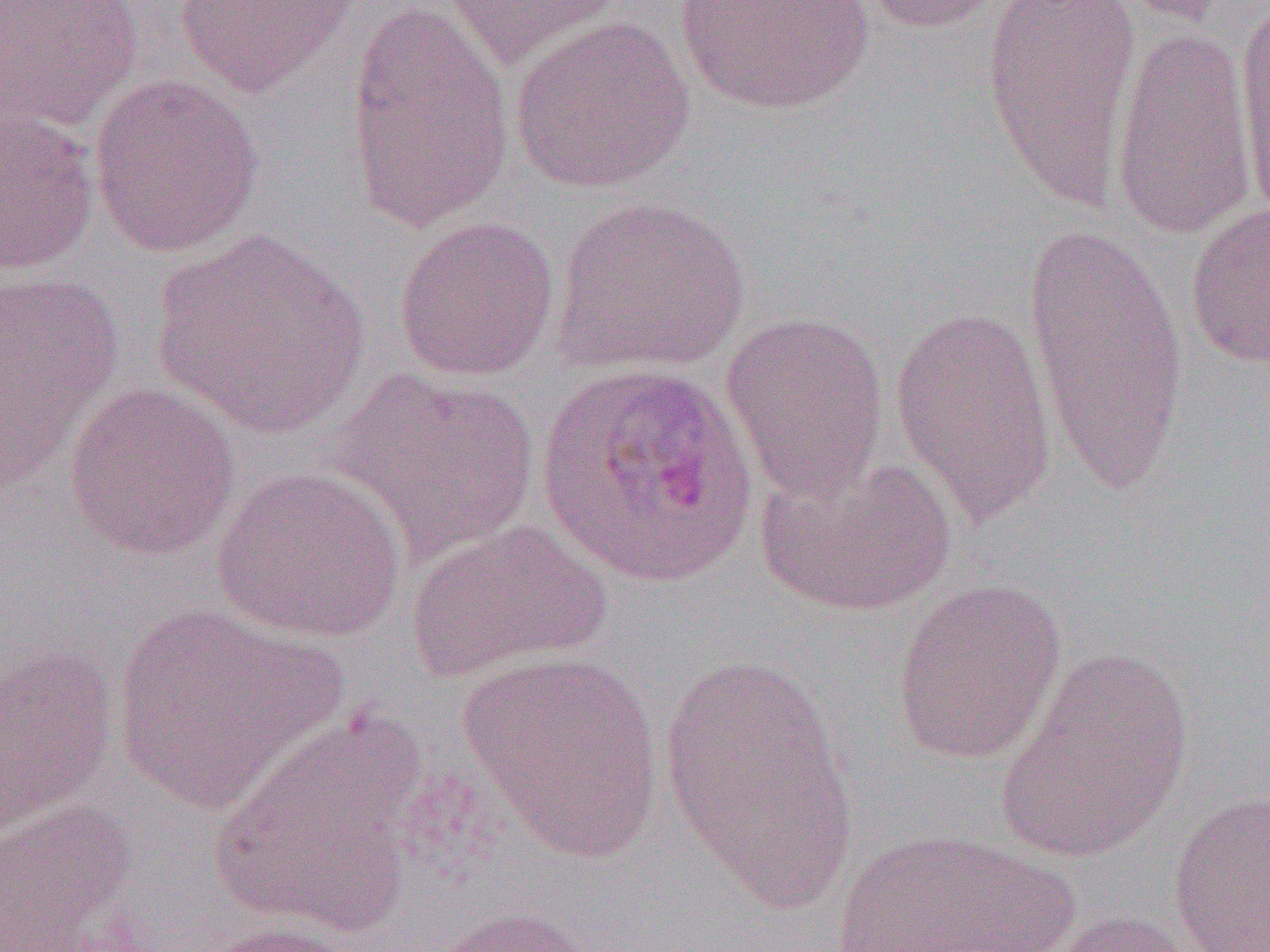
slide_level_diagnosis: Plasmodium ovale
field_of_view: one of a larger specimen
modality: light microscopy
uninfected_red_blood_cell_locations: 'approximate bounding boxes as [x1, y1, x2, y2] in pixels: [0, 0, 143, 133], [171, 0, 362, 96], [344, 0, 515, 233], [671, 0, 878, 116], [853, 0, 1011, 34], [980, 0, 1142, 213], [1102, 0, 1236, 26], [1233, 0, 1270, 222], [438, 1, 626, 71], [508, 16, 695, 195], [1109, 24, 1257, 242], [88, 74, 265, 257], [0, 100, 99, 277], [551, 196, 752, 377], [1185, 200, 1269, 371], [392, 215, 560, 381], [1023, 218, 1190, 501], [153, 228, 371, 438], [0, 266, 125, 483], [888, 307, 1057, 528], [721, 310, 890, 499], [333, 369, 541, 563], [63, 381, 241, 560], [752, 451, 955, 617], [211, 465, 407, 643], [405, 519, 612, 683], [892, 578, 1067, 766], [111, 601, 344, 813], [0, 640, 118, 836], [996, 647, 1195, 863], [459, 651, 665, 861], [660, 653, 856, 909], [214, 713, 426, 940], [1167, 790, 1269, 951], [0, 802, 139, 951], [823, 828, 1079, 951], [426, 904, 608, 952], [1045, 910, 1201, 952], [181, 921, 363, 952]'
magnification: 1000x
image_size: 1270×952 pixels
preparation: thin blood film
plasmodium_ovale_infected_red_blood_cell_locations: 'approximate bounding boxes as [x1, y1, x2, y2] in pixels: [536, 360, 758, 589]'